Assess the morphology of the red blood cells.
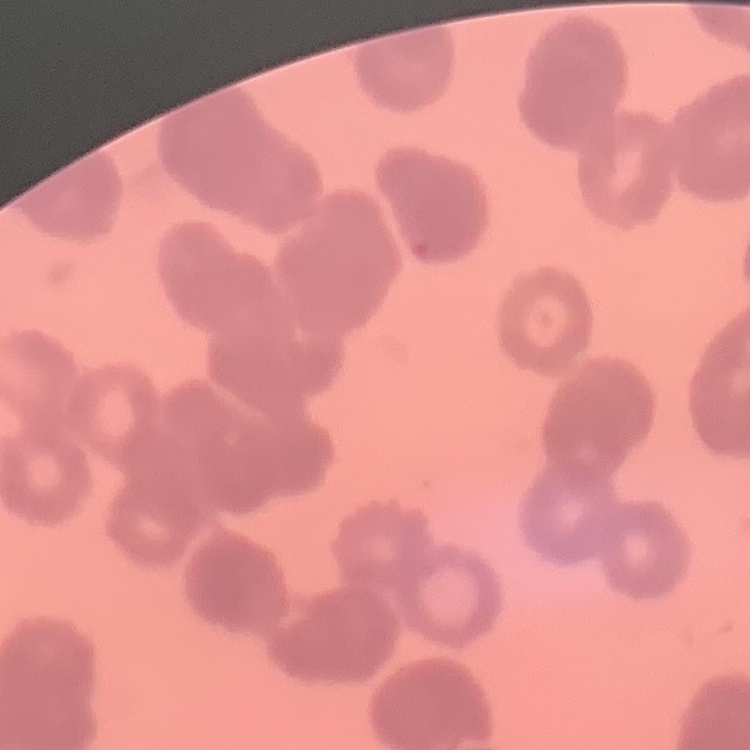
They show rouleaux formation.

Thin blood smear. Field's or Giemsa stain. One tile cut from a larger photomicrograph.